State the blood parasite species.
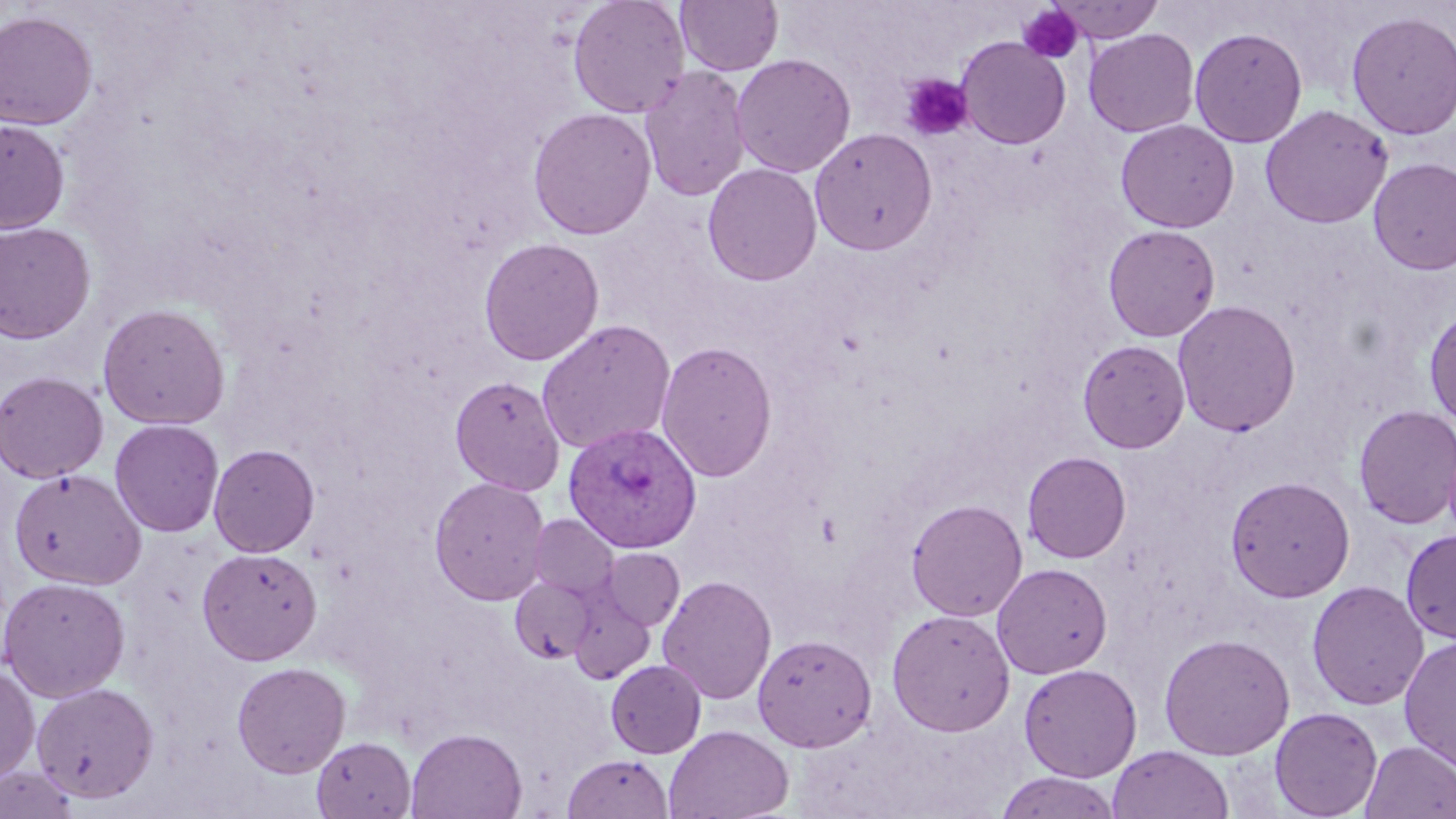
Plasmodium vivax.

uninfected red blood cell locations = approximate bounding boxes as [x1, y1, x2, y2] in pixels: [567, 0, 690, 118], [676, 0, 783, 76], [1050, 0, 1165, 43], [0, 10, 98, 130], [1345, 10, 1456, 140], [1189, 27, 1308, 147], [1084, 29, 1200, 137], [956, 37, 1071, 149], [731, 53, 856, 178], [639, 65, 752, 202], [1259, 104, 1393, 229], [528, 107, 656, 240], [0, 119, 70, 234], [1115, 119, 1239, 233], [810, 128, 937, 256], [1368, 157, 1456, 274], [703, 162, 822, 287], [0, 221, 96, 344], [1103, 224, 1220, 341], [478, 237, 604, 366], [1172, 299, 1302, 437], [96, 303, 231, 430], [1424, 305, 1456, 429], [536, 319, 676, 455], [1077, 339, 1189, 452], [656, 340, 777, 483], [0, 371, 109, 483], [450, 374, 565, 495], [1353, 404, 1456, 530], [110, 419, 224, 537], [209, 443, 320, 557], [1022, 451, 1131, 563], [9, 468, 146, 590], [1225, 475, 1355, 602], [429, 476, 550, 605], [906, 499, 1028, 621], [528, 515, 618, 600], [1400, 528, 1456, 645], [197, 547, 322, 665], [600, 549, 684, 631], [992, 562, 1112, 679], [657, 574, 777, 705], [509, 575, 599, 665], [0, 576, 130, 702], [1307, 579, 1429, 710], [567, 587, 657, 683], [887, 608, 1015, 736], [1158, 632, 1295, 760], [752, 633, 876, 751], [1399, 635, 1456, 771], [606, 659, 706, 758], [231, 661, 350, 777], [0, 663, 40, 784], [1018, 663, 1142, 782], [30, 682, 160, 803], [1269, 706, 1383, 819], [663, 725, 794, 819], [407, 728, 526, 819], [312, 736, 416, 819], [1360, 740, 1456, 818], [1108, 744, 1234, 819], [563, 753, 673, 818], [0, 764, 80, 819], [994, 772, 1121, 819]
magnification = 1000x
Plasmodium vivax-infected red blood cell locations = approximate bounding boxes as [x1, y1, x2, y2] in pixels: [563, 422, 701, 553]
image size = 1456×819 pixels
modality = light microscopy
stain = May-Grünwald-Giemsa
platelet locations = approximate bounding boxes as [x1, y1, x2, y2] in pixels: [1018, 5, 1084, 64], [900, 74, 973, 141]
field of view = one of a larger specimen
preparation = thin blood film